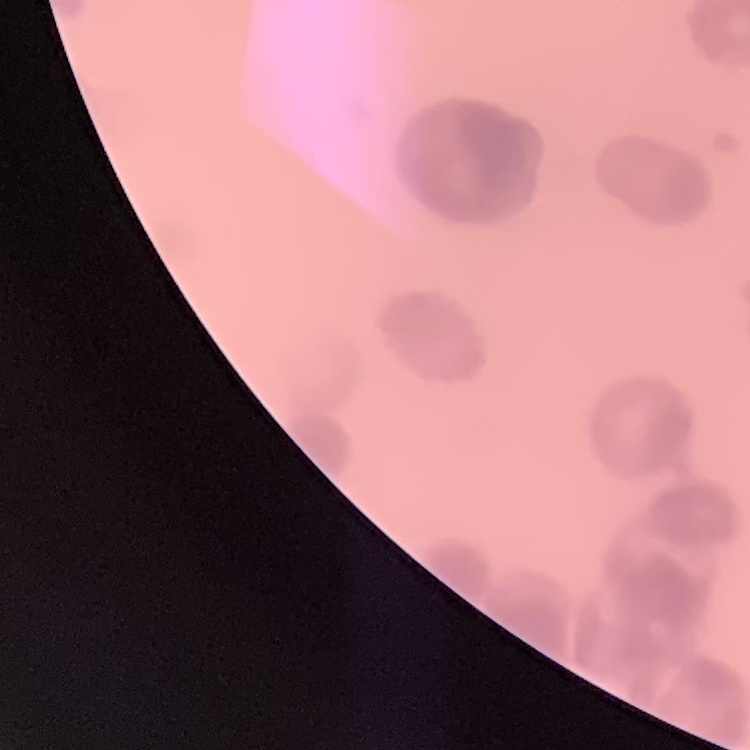

red_blood_cell_morphology: rouleaux formation
image_type: one tile cut from a larger photomicrograph
preparation: thin peripheral smear
stain: Field's or Giemsa